State which cell type is depicted.
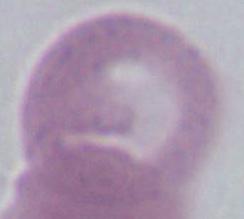
This is an erythrocyte.

modality: photomicrograph
magnification: 1000x